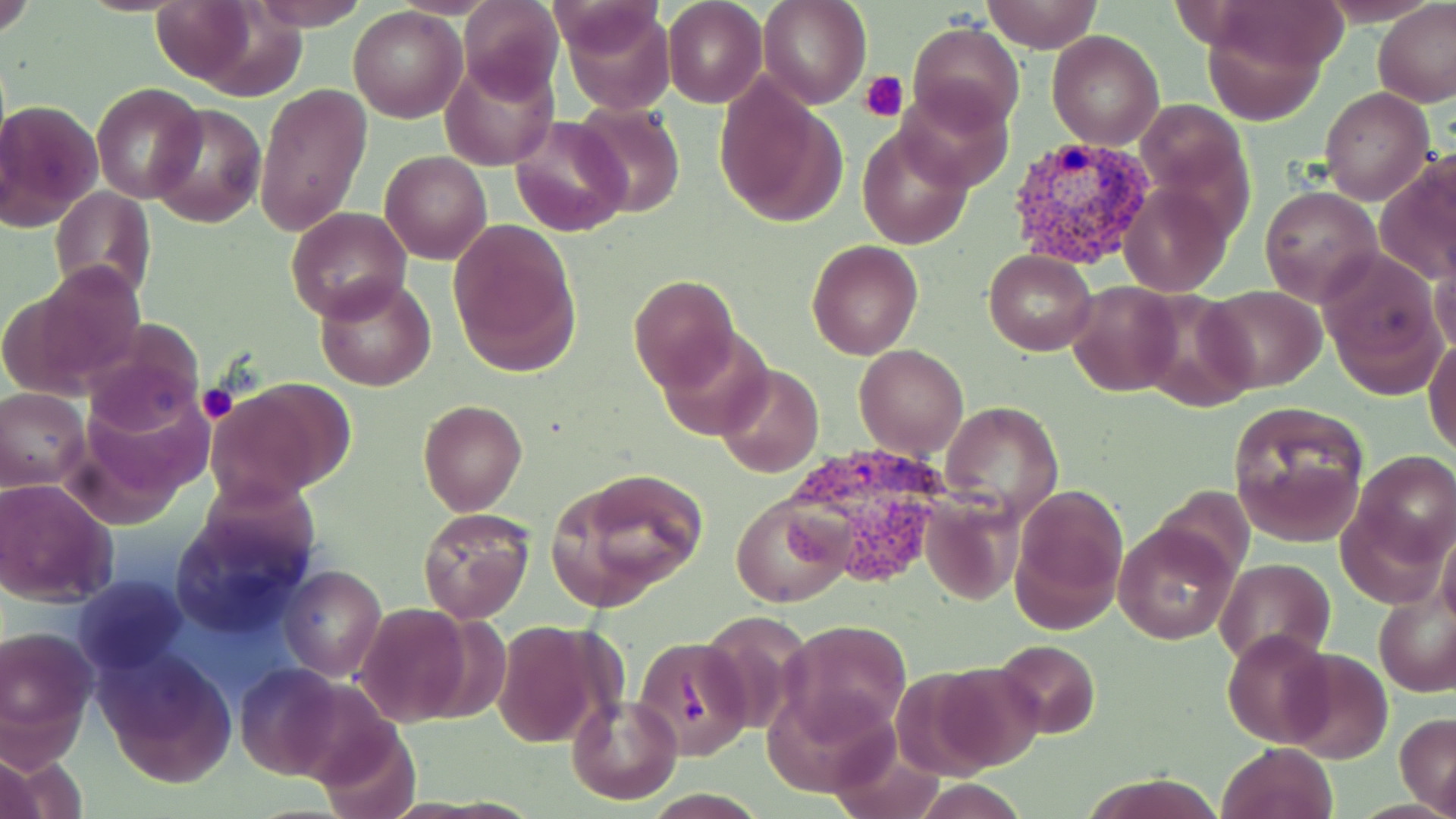
Plasmodium vivax-infected red blood cell locations = approximate bounding boxes as (x1,y1)-(x2,y2) corner pairs in pixels: (1005,136)-(1157,266), (778,445)-(961,596)
slide-level diagnosis = Plasmodium vivax
magnification = 1000x
image size = 1456×819 pixels
uninfected red blood cell locations = approximate bounding boxes as (x1,y1)-(x2,y2) corner pairs in pixels: (0,0)-(38,40), (153,0)-(256,85), (250,0)-(370,30), (460,0)-(563,105), (662,0)-(767,108), (758,0)-(870,109), (982,0)-(1100,54), (1373,1)-(1455,107), (559,4)-(675,114), (348,6)-(467,123), (1202,14)-(1330,126), (909,21)-(1024,133), (1047,29)-(1164,149), (441,55)-(558,171), (715,78)-(841,226), (896,80)-(1014,195), (255,82)-(372,237), (93,83)-(205,203), (1320,87)-(1432,203), (1,97)-(104,234), (1139,99)-(1249,204), (149,103)-(265,227), (571,103)-(686,219), (509,114)-(634,237), (858,128)-(972,252), (380,151)-(492,264), (1377,160)-(1455,287), (1117,180)-(1233,297), (48,185)-(156,304), (1259,186)-(1384,307), (286,206)-(412,322), (447,216)-(580,373), (807,239)-(924,361), (983,250)-(1098,354), (1321,252)-(1443,391), (1432,257)-(1456,360), (12,259)-(150,397), (313,275)-(436,391), (630,276)-(739,392), (1066,281)-(1183,398), (1201,284)-(1327,392), (1129,292)-(1256,411), (80,320)-(205,437), (656,326)-(774,442), (1424,337)-(1456,457), (855,345)-(969,460), (716,364)-(823,478), (209,381)-(348,505), (1,388)-(88,489), (940,399)-(1065,518), (418,400)-(528,516), (1230,403)-(1369,548), (1356,450)-(1455,561), (556,470)-(708,608), (1,477)-(119,606), (1012,483)-(1128,630), (732,496)-(850,607), (920,497)-(1022,606), (417,506)-(535,625), (1113,522)-(1236,643), (1214,557)-(1335,666), (279,566)-(386,682), (75,575)-(184,672), (1375,590)-(1455,698), (354,603)-(475,725), (781,619)-(912,740), (493,622)-(605,750), (1,623)-(96,754), (1224,626)-(1333,746), (635,634)-(752,761), (993,639)-(1100,740), (97,650)-(237,789), (1284,650)-(1394,763), (233,664)-(355,783), (927,664)-(1049,772), (565,693)-(682,804), (1396,712)-(1456,814), (314,719)-(421,819), (1217,741)-(1339,819), (0,754)-(56,819), (1086,773)-(1220,818)
field of view = single
modality = optical microscopy
platelet locations = approximate bounding boxes as (x1,y1)-(x2,y2) corner pairs in pixels: (859,70)-(910,119), (198,385)-(237,422)
stain = May-Grünwald-Giemsa
preparation = thin blood film